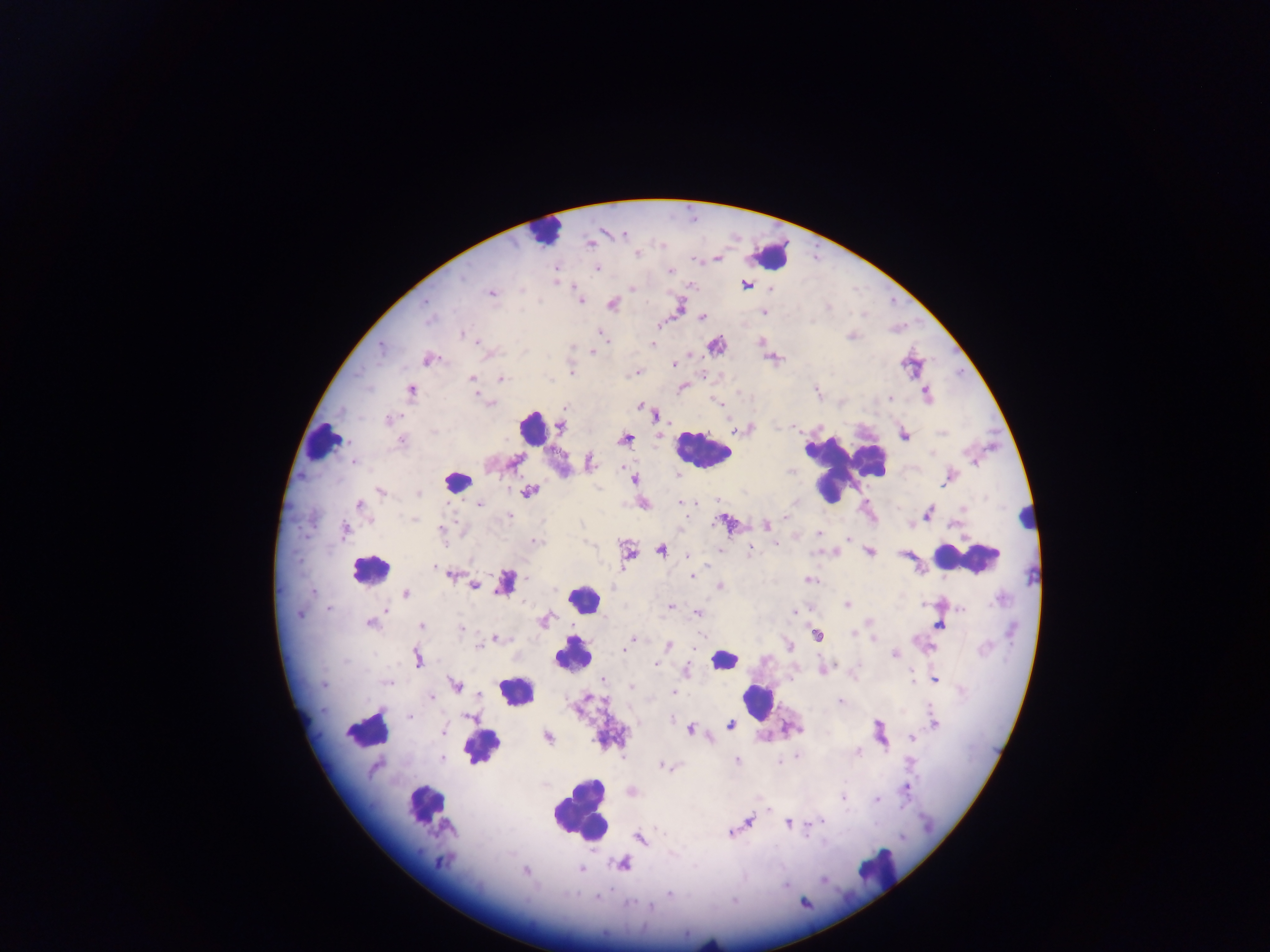

{
  "preparation": "thick blood smear",
  "leukocyte_locations": "approximate centers as (x, y) in pixels: (542, 233), (773, 256), (533, 429), (322, 441), (703, 450), (836, 467), (457, 482), (1027, 517), (966, 558), (369, 570), (582, 599), (573, 655), (723, 660), (516, 692), (756, 700), (369, 727), (480, 745), (425, 802), (578, 810), (879, 865)",
  "country": "Ghana",
  "field_of_view": "single",
  "plasmodium_parasite_locations": "approximate centers as (x, y) in pixels: (624, 235), (591, 244), (637, 255), (598, 269), (670, 270), (461, 278), (746, 285), (632, 288), (521, 289), (491, 294), (581, 301), (426, 302), (612, 304), (764, 312), (703, 317), (428, 320), (464, 335), (606, 339), (478, 342), (652, 343), (381, 346), (592, 351), (428, 359), (673, 364), (571, 372), (637, 372), (502, 378), (471, 379), (411, 390), (816, 390), (926, 392), (890, 398), (482, 400), (717, 402), (491, 403), (640, 406), (654, 415), (388, 419), (560, 427), (434, 432), (904, 436), (625, 438), (402, 441), (353, 462), (516, 462), (589, 462), (623, 467), (677, 474), (635, 479), (381, 491), (530, 492), (418, 494), (680, 502), (480, 505), (360, 506), (928, 513), (510, 516), (786, 517), (415, 520), (766, 525), (344, 531), (440, 531), (818, 533), (849, 538), (535, 541), (775, 544), (719, 549), (661, 550), (750, 552), (869, 553), (627, 555), (688, 555), (435, 567), (451, 575), (693, 576), (526, 578), (809, 580), (504, 583), (474, 585), (720, 587), (405, 594), (847, 605), (670, 606), (329, 610), (385, 610), (961, 610), (696, 612), (794, 612), (299, 614), (544, 621), (371, 624), (421, 625), (939, 626), (461, 629), (853, 634), (817, 635), (701, 636), (496, 639), (631, 639), (873, 639), (668, 646), (789, 646), (480, 647), (626, 649), (894, 654), (417, 659), (655, 664), (686, 671), (911, 671), (603, 679), (934, 679), (387, 683), (323, 684), (455, 684), (630, 686), (673, 692), (479, 695), (431, 697), (840, 701), (409, 716), (469, 716), (935, 723), (730, 724), (690, 729), (444, 732), (548, 737), (912, 738), (858, 751), (797, 756), (442, 759), (737, 760), (780, 762), (662, 765), (374, 768), (907, 788), (843, 797), (876, 800), (749, 821), (822, 821), (788, 824), (731, 833), (639, 839), (441, 862), (622, 863), (581, 869), (525, 872), (823, 880), (786, 886), (670, 894), (597, 897), (734, 900), (629, 903), (650, 906)",
  "capture": "mobile-phone photograph through a microscope",
  "image_size": "1270×952 pixels"
}